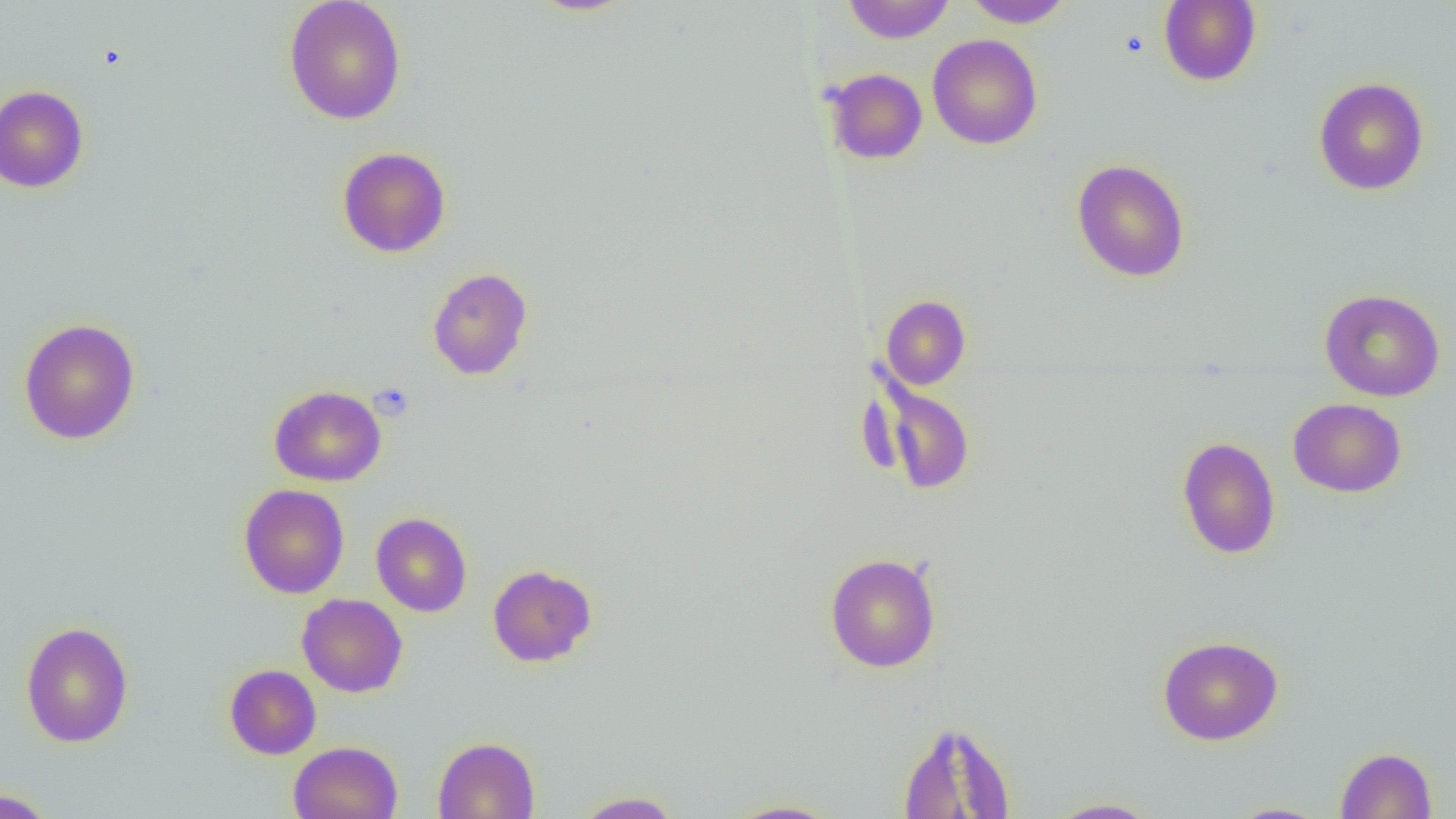

slide_level_diagnosis: no evidence of blood parasites
image_size: 1456×819 pixels
magnification: 1000x
field_of_view: one of a larger specimen
platelet_locations: 'approximate bounding boxes as (x1, y1, x2, y2) in pixels: (369, 382, 415, 421)'
preparation: thin blood smear
uninfected_red_blood_cell_locations: 'approximate bounding boxes as (x1, y1, x2, y2) in pixels: (283, 0, 407, 125), (843, 0, 954, 43), (963, 0, 1073, 28), (1159, 0, 1261, 87), (927, 33, 1043, 150), (825, 68, 927, 164), (1313, 77, 1429, 195), (0, 85, 89, 193), (337, 146, 451, 258), (1071, 159, 1190, 282), (427, 267, 532, 380), (1319, 288, 1445, 402), (881, 295, 970, 389), (18, 318, 140, 445), (867, 374, 978, 496), (269, 385, 386, 486), (1288, 398, 1406, 497), (1177, 436, 1280, 559), (238, 483, 349, 599), (371, 512, 472, 617), (824, 552, 941, 673), (487, 564, 597, 667), (297, 593, 408, 697), (20, 621, 134, 747), (1157, 635, 1284, 745), (224, 664, 321, 759), (896, 719, 1017, 818), (432, 736, 540, 819), (288, 741, 403, 819), (1335, 747, 1437, 818), (0, 788, 58, 818), (571, 790, 684, 818), (1044, 797, 1162, 818), (722, 798, 844, 818), (1223, 802, 1335, 818)'
modality: light microscopy